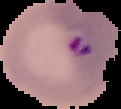

From a thin blood film. Malaria status: parasitized. Image is 121×109 pixels. Cell region segmented out of the field of view; the surrounding area is masked to black.